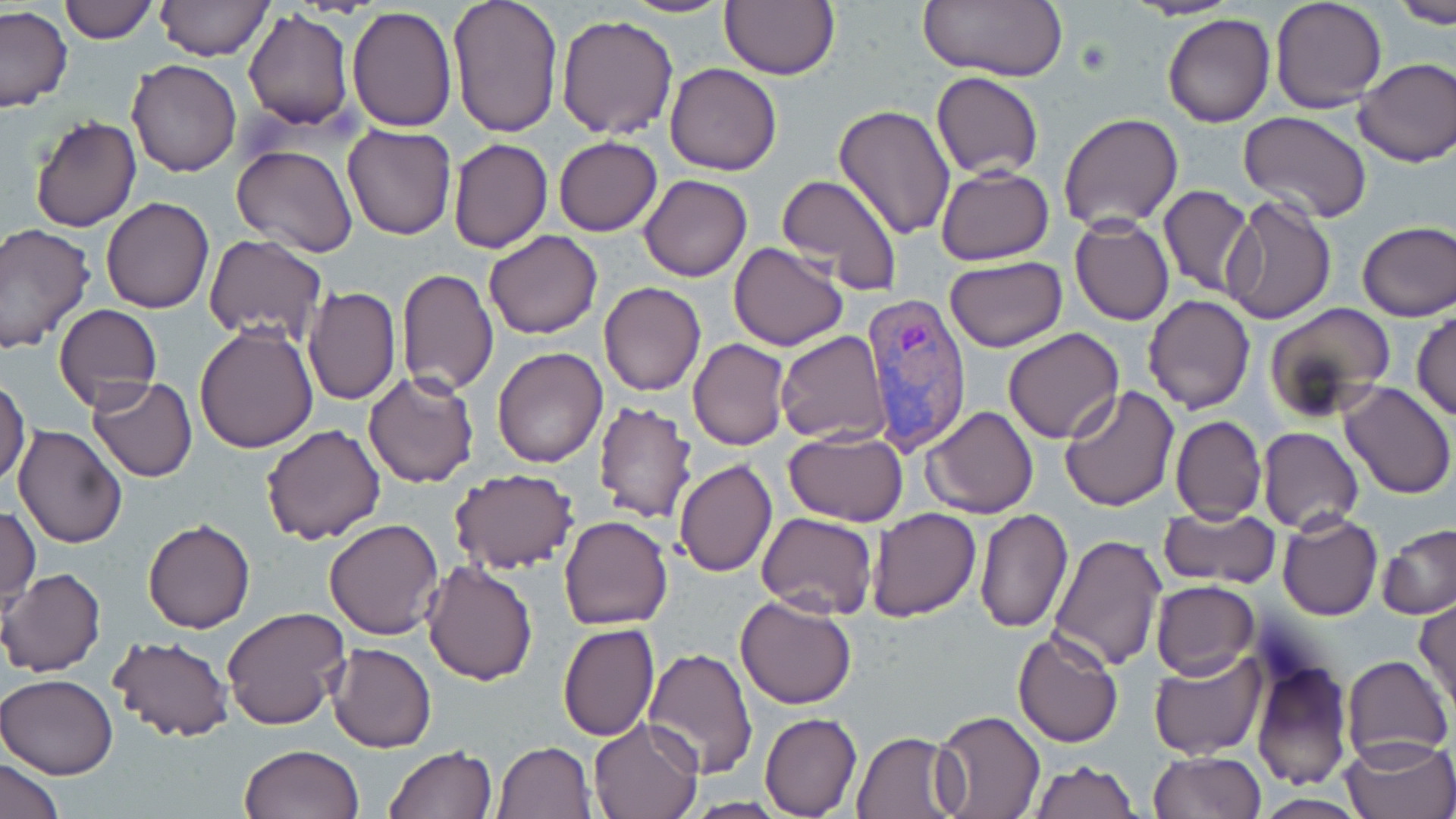

slide-level diagnosis = Plasmodium vivax
magnification = 1000x
stain = May-Grünwald-Giemsa
preparation = thin blood smear
Plasmodium vivax-infected red blood cell locations = approximate bounding boxes as (x1,y1)-(x2,y2) corner pairs in pixels: (860,287)-(973,452)
uninfected red blood cell locations = approximate bounding boxes as (x1,y1)-(x2,y2) corner pairs in pixels: (59,0)-(158,43), (153,0)-(273,60), (447,0)-(563,137), (617,0)-(738,17), (916,0)-(1070,83), (1125,0)-(1238,20), (1390,0)-(1456,25), (719,1)-(840,80), (1269,1)-(1389,114), (0,5)-(74,114), (347,5)-(458,132), (242,7)-(354,132), (554,13)-(679,139), (1163,13)-(1275,128), (1354,57)-(1456,166), (126,60)-(242,177), (665,63)-(782,175), (932,71)-(1043,179), (833,104)-(957,240), (1238,111)-(1371,223), (1059,112)-(1184,230), (28,115)-(142,233), (341,123)-(455,241), (552,137)-(662,236), (448,138)-(554,255), (232,146)-(359,259), (936,166)-(1054,265), (774,173)-(904,296), (639,174)-(752,282), (1157,185)-(1255,298), (1221,192)-(1337,322), (101,197)-(213,314), (1069,216)-(1175,325), (1355,220)-(1456,320), (0,223)-(97,354), (483,231)-(602,340), (203,234)-(328,344), (727,242)-(848,350), (944,256)-(1068,351), (396,267)-(498,396), (599,282)-(706,396), (303,285)-(401,405), (1143,294)-(1255,414), (55,303)-(162,412), (1263,303)-(1397,426), (1413,311)-(1456,422), (194,323)-(317,453), (1004,328)-(1123,443), (776,331)-(890,444), (688,339)-(790,451), (492,347)-(607,468), (363,370)-(479,488), (85,378)-(198,482), (1,379)-(31,487), (1339,382)-(1454,499), (1060,387)-(1180,511), (590,400)-(699,522), (922,405)-(1039,519), (1170,414)-(1267,524), (260,423)-(385,545), (12,424)-(127,548), (1258,427)-(1364,533), (784,429)-(909,525), (675,460)-(776,577), (448,467)-(579,576), (1157,504)-(1280,589), (1,506)-(39,612), (867,507)-(980,621), (974,508)-(1073,633), (757,512)-(877,618), (1277,512)-(1382,620), (560,515)-(672,631), (324,518)-(445,640), (143,519)-(255,634), (1378,523)-(1456,620), (1047,532)-(1166,673), (422,561)-(539,684), (1,569)-(106,677), (1151,581)-(1259,679), (734,594)-(858,710), (1414,597)-(1456,714), (221,606)-(351,732), (557,622)-(660,741), (1013,628)-(1124,748), (108,635)-(233,744), (327,642)-(438,753), (643,647)-(757,777), (1148,650)-(1269,761), (1341,654)-(1452,764), (1247,659)-(1353,790), (0,674)-(120,780), (933,709)-(1045,818), (759,712)-(861,817), (588,717)-(702,819), (852,730)-(962,818), (1337,737)-(1455,819), (494,741)-(595,819), (238,744)-(364,819), (383,746)-(497,819), (1149,750)-(1267,818), (2,756)-(66,819), (1028,760)-(1139,818), (1253,794)-(1369,818), (684,799)-(792,818)
image size = 1456×819 pixels
field of view = single
modality = optical microscopy